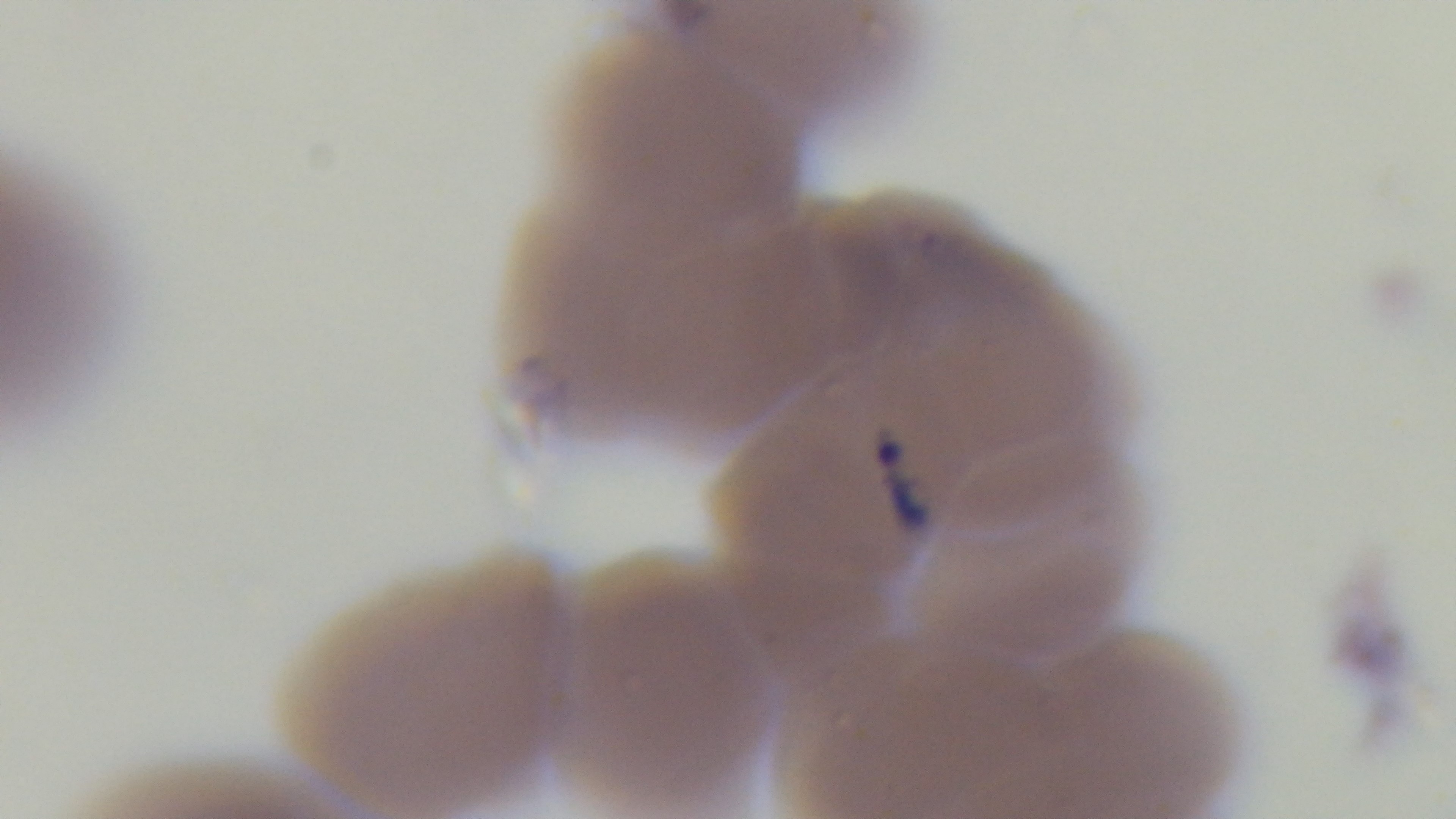
100x oil-immersion objective. Single field of view. Giemsa-stained. Light microscopy. Preparation: thin. Malaria status: positive. Captured with a mounted 4K digital camera.